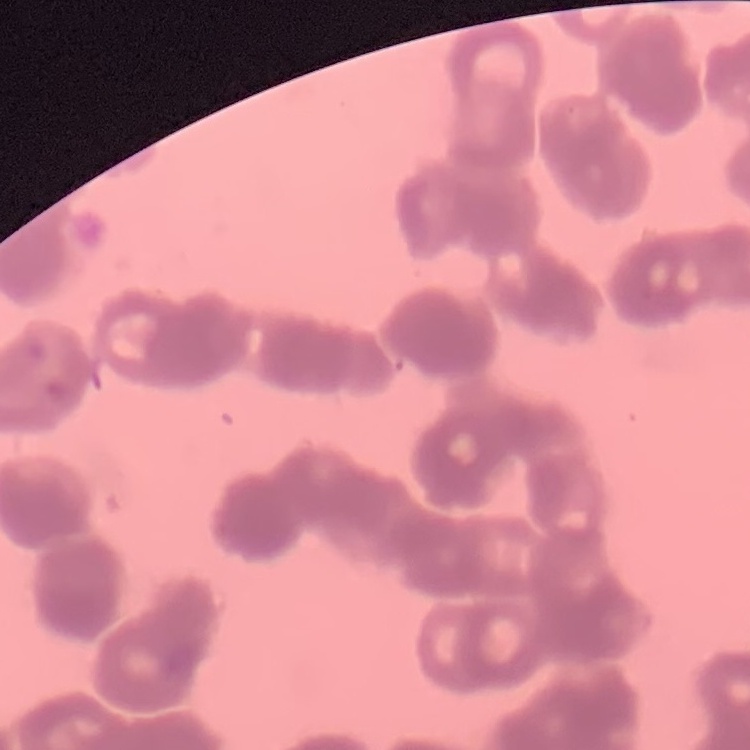
Summary:
  - Erythrocyte morphology: rouleaux formation
  - Stain: Field's or Giemsa
  - Image type: square crop of a larger photomicrograph
  - Preparation: thin blood smear